Report the malaria status of this cell.
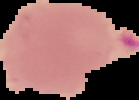

It is uninfected.

image size = 139×100 pixels
preparation = thin blood smear
image type = segmented cell region on a black background